Outline each white blood cell.
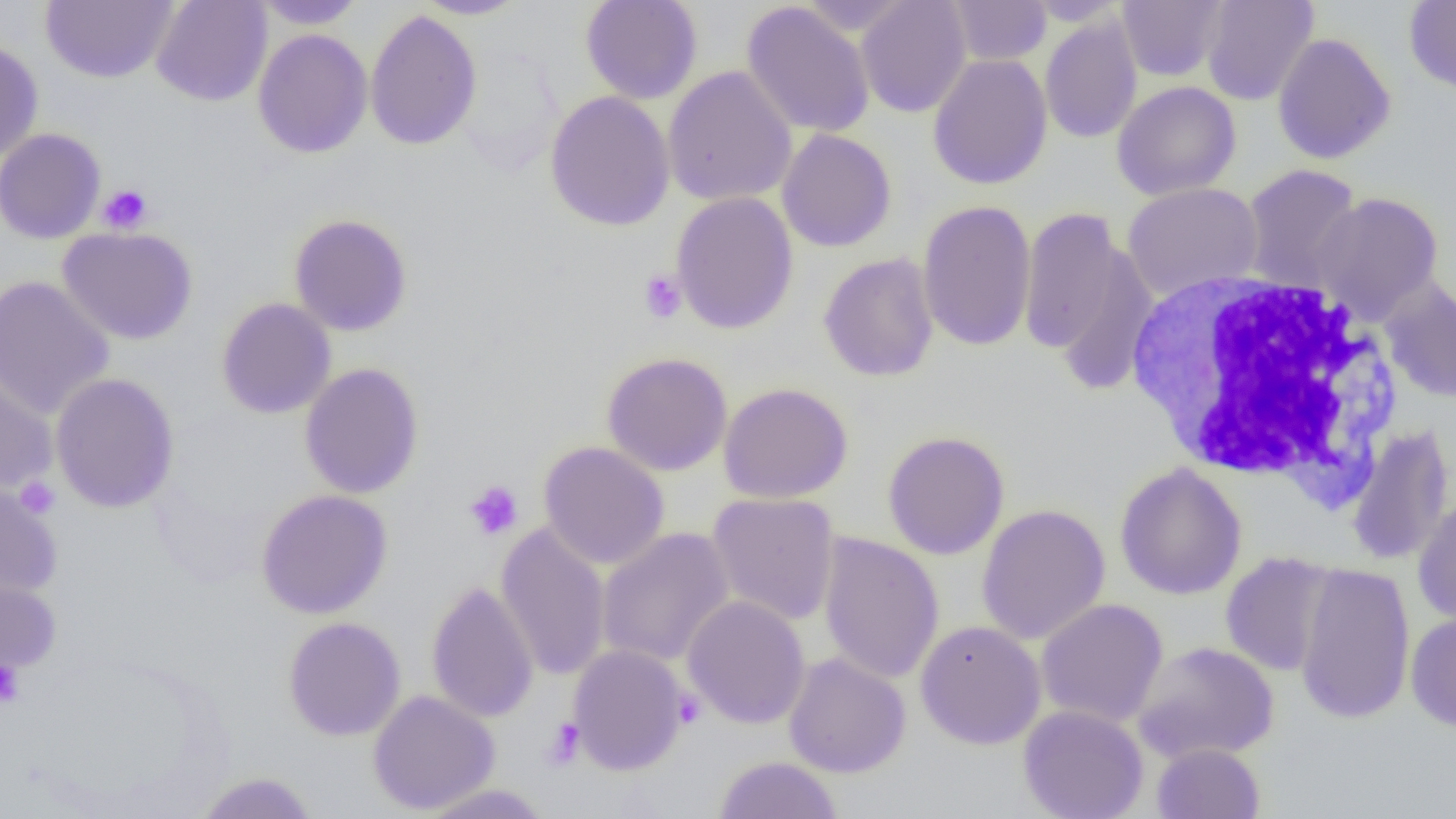
Approximate bounding boxes as (x1, y1, x2, y2) in pixels.
White blood cells: (1121, 269, 1404, 497).

Summary:
  - Uninfected red blood cell locations: (151, 0, 272, 107), (412, 0, 528, 19), (580, 0, 703, 104), (795, 0, 918, 36), (856, 0, 971, 118), (947, 0, 1052, 66), (1023, 0, 1130, 25), (1117, 0, 1227, 81), (1201, 0, 1318, 106), (1404, 0, 1456, 96), (40, 1, 178, 84), (252, 1, 367, 30), (741, 2, 875, 138), (365, 9, 482, 151), (1039, 16, 1142, 144), (252, 28, 373, 158), (1272, 33, 1396, 165), (0, 40, 44, 161), (928, 54, 1053, 190), (662, 66, 798, 207), (1112, 81, 1241, 201), (545, 90, 676, 232), (0, 128, 106, 244), (777, 128, 896, 252), (1241, 164, 1363, 293), (1122, 182, 1264, 301), (1311, 191, 1445, 323), (670, 192, 799, 335), (917, 199, 1037, 352), (1019, 206, 1137, 363), (288, 213, 413, 336), (57, 226, 199, 345), (1048, 244, 1160, 398), (818, 252, 940, 383), (0, 275, 115, 421), (1379, 277, 1456, 405), (216, 297, 337, 419), (601, 351, 733, 476), (299, 363, 424, 499), (0, 368, 58, 497), (50, 372, 180, 514), (718, 382, 854, 504), (1345, 423, 1455, 568), (882, 430, 1010, 560), (538, 441, 670, 569), (1115, 462, 1247, 600), (0, 481, 63, 601), (256, 488, 393, 619), (706, 492, 840, 626), (1413, 495, 1456, 626), (976, 504, 1111, 646), (496, 524, 611, 681), (596, 527, 735, 667), (818, 532, 944, 685), (1220, 552, 1338, 677), (1294, 562, 1416, 725), (0, 577, 61, 677), (426, 580, 539, 723), (682, 595, 811, 729), (1035, 598, 1168, 728), (1406, 613, 1456, 732), (283, 616, 406, 741), (915, 620, 1046, 749), (1132, 640, 1279, 764), (567, 644, 690, 775), (783, 652, 911, 778), (368, 690, 500, 815), (1017, 705, 1149, 819), (1151, 742, 1265, 819), (713, 756, 844, 819), (194, 771, 319, 818), (417, 783, 555, 818)
  - Platelet locations: (98, 183, 153, 234), (638, 270, 687, 324), (14, 476, 61, 519), (464, 480, 524, 541), (0, 660, 24, 709), (672, 690, 704, 728), (543, 717, 585, 770)
  - Slide-level diagnosis: negative for blood parasites
  - Magnification: 1000x
  - Modality: optical microscopy
  - Image size: 1456×819 pixels
  - Field of view: one of a larger specimen
  - Preparation: thin blood smear